Classify this cell by malaria status.
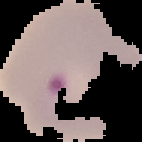

Parasitized.

The area outside the segmented cell region is set to black. From a thin blood smear. Image is 142×142 pixels.